Assess this cell for malaria.
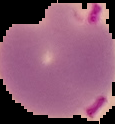

Parasitized.

Summary:
  - Image type: cell region segmented out of the field of view; surrounding area masked to black
  - Preparation: thin blood film
  - Image size: 115×124 pixels